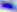 Toxoplasma gondii is shown. Captured at 400x magnification. Photomicrograph.